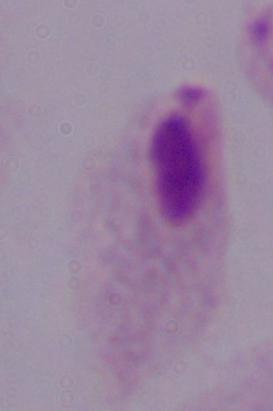
Micrograph. A trichomonad is shown. 1000x magnification.